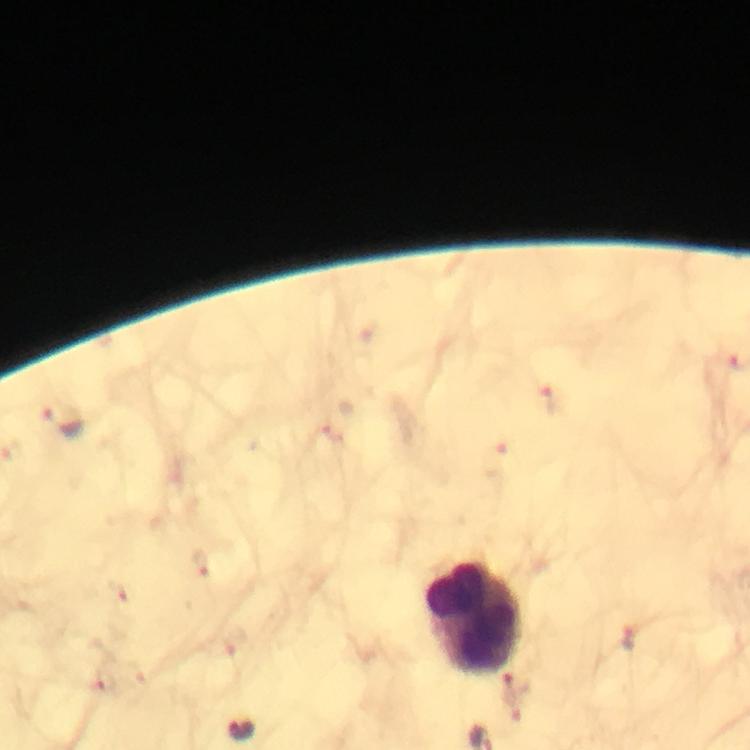
Approximate centers as {x, y} in pixels. Malaria parasite locations: {550, 400}, {64, 421}, {629, 636}, {516, 687}, {243, 730}. Leukocyte locations: {472, 617}. Smartphone photograph taken through a microscope. Cropped region of a single field of view. Immersion oil was used. Image is 750×750 pixels. Giemsa stain. Thick smear. 100x magnification. From a malaria diagnostic workup.